Evaluate for Plasmodium parasites.
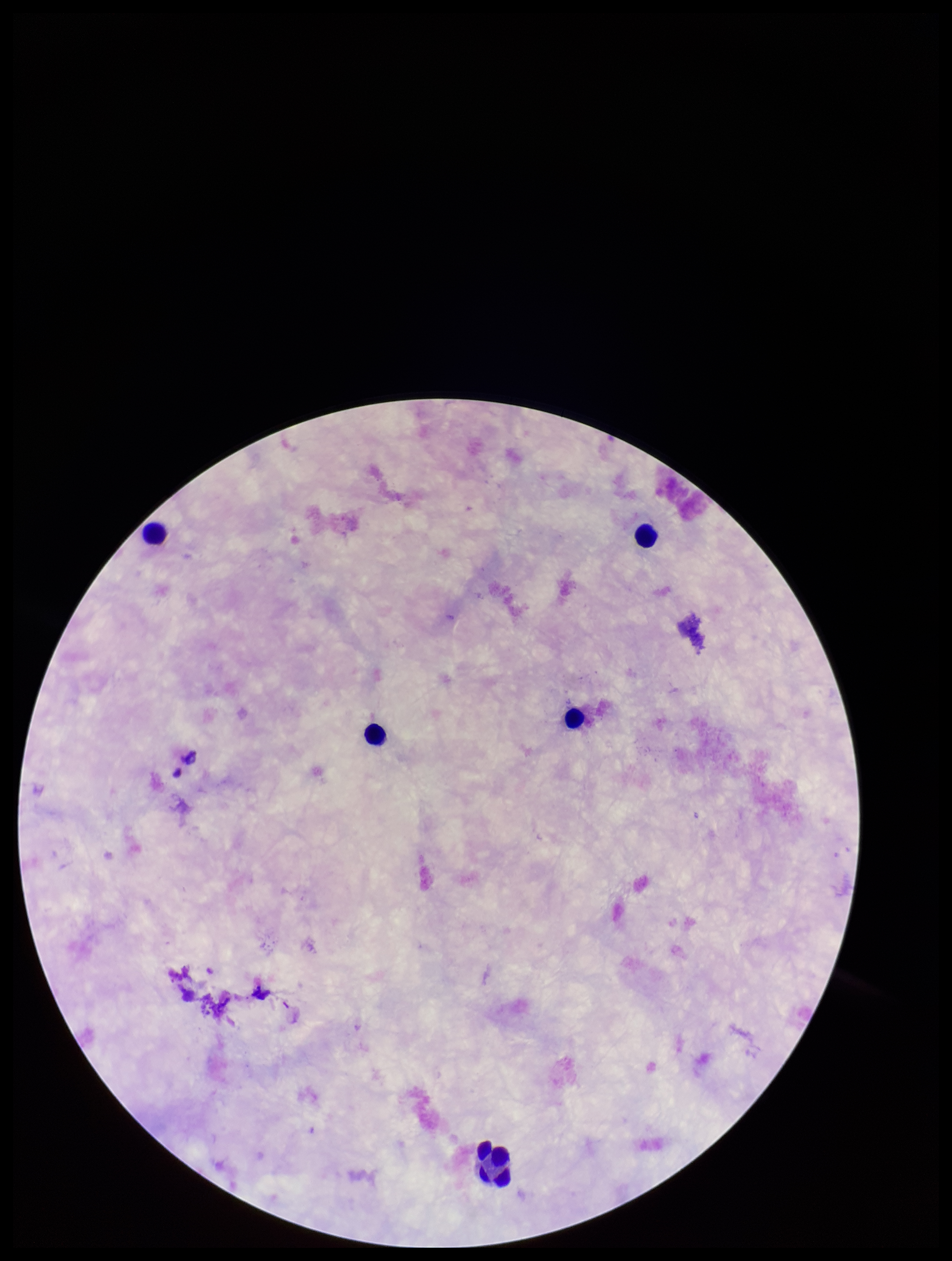
None seen.

{
  "parasite_count": 0,
  "preparation": "thick",
  "patient_malaria_status": "negative",
  "image_size": "952×1261 pixels",
  "field_of_view": "one from this slide",
  "stain": "Giemsa",
  "capture": "smartphone photograph through the microscope eyepiece",
  "leukocyte_count": 5
}